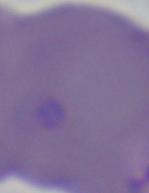

Photomicrograph. A Babesia parasite is shown. Captured at 1000x magnification.